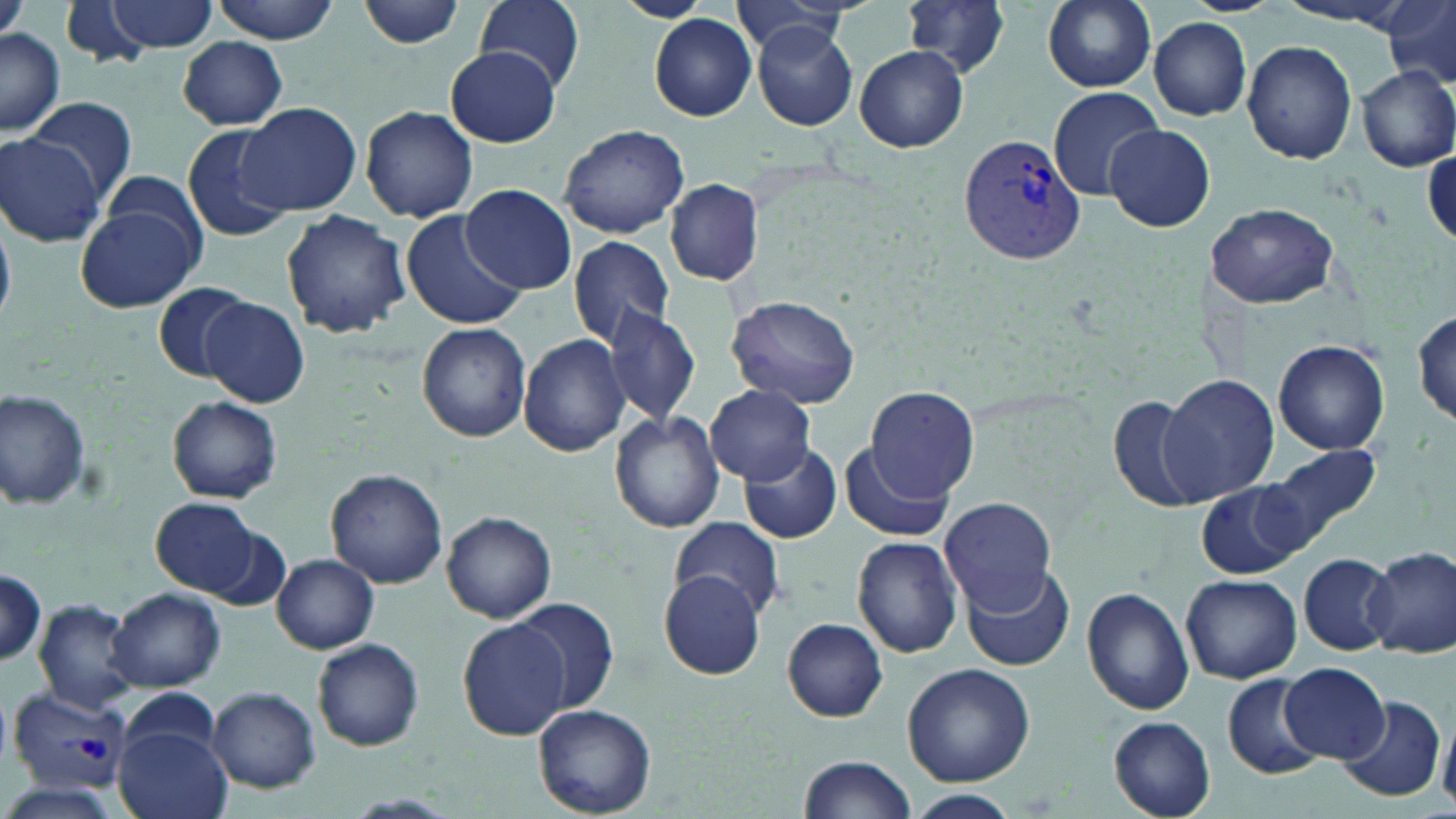

Summary:
  - Coordinate format: approximate bounding boxes as [x1, y1, x2, y2] in pixels
  - Uninfected red blood cell locations: [0, 0, 28, 46], [102, 0, 218, 53], [210, 0, 339, 43], [357, 0, 469, 49], [478, 0, 585, 91], [617, 0, 709, 22], [727, 0, 855, 58], [898, 0, 1013, 79], [1040, 0, 1156, 91], [59, 1, 156, 66], [1381, 4, 1456, 86], [649, 13, 757, 121], [1150, 17, 1252, 121], [750, 22, 860, 130], [0, 29, 63, 135], [176, 38, 289, 128], [1242, 39, 1358, 164], [855, 45, 968, 153], [445, 46, 562, 147], [1355, 65, 1455, 172], [1048, 86, 1166, 200], [26, 96, 137, 204], [237, 101, 362, 217], [358, 104, 480, 222], [182, 123, 294, 242], [559, 124, 689, 239], [1105, 125, 1212, 231], [0, 133, 106, 248], [97, 170, 210, 264], [664, 179, 764, 286], [459, 184, 577, 296], [1206, 201, 1338, 310], [77, 205, 199, 313], [402, 209, 526, 330], [280, 210, 410, 339], [567, 235, 674, 348], [152, 281, 256, 382], [727, 294, 861, 408], [201, 297, 310, 408], [602, 303, 701, 428], [1413, 306, 1455, 427], [415, 322, 532, 442], [518, 334, 630, 456], [1272, 339, 1391, 455], [1160, 373, 1280, 506], [861, 384, 979, 500], [706, 385, 814, 483], [2, 391, 93, 511], [1100, 393, 1204, 515], [165, 395, 283, 504], [610, 411, 726, 532], [737, 439, 843, 545], [845, 441, 955, 542], [1260, 442, 1383, 553], [327, 468, 448, 588], [1197, 482, 1310, 580], [940, 496, 1058, 614], [151, 497, 265, 598], [443, 510, 555, 623], [669, 518, 786, 618], [851, 534, 964, 659], [1367, 546, 1456, 658], [1299, 552, 1397, 655], [272, 554, 379, 654], [960, 562, 1076, 673], [0, 567, 46, 668], [657, 568, 770, 680], [1181, 574, 1302, 684], [1081, 586, 1194, 717], [108, 587, 225, 692], [32, 598, 138, 713], [509, 599, 622, 716], [458, 618, 572, 739], [781, 619, 890, 721], [312, 639, 424, 751], [1282, 661, 1389, 762], [902, 662, 1035, 787], [1223, 674, 1324, 778], [206, 686, 321, 793], [119, 689, 219, 765], [1337, 695, 1447, 802], [534, 704, 657, 818], [1439, 706, 1456, 812], [1108, 716, 1214, 817], [116, 726, 232, 819], [798, 754, 918, 818], [905, 790, 1019, 819]
  - Plasmodium vivax-infected red blood cell locations: [958, 131, 1087, 265], [5, 687, 132, 794]
  - Slide-level diagnosis: Plasmodium vivax
  - Preparation: thin blood smear
  - Image size: 1456×819 pixels
  - Magnification: 1000x
  - Field of view: single
  - Stain: May-Grünwald-Giemsa
  - Modality: optical microscopy